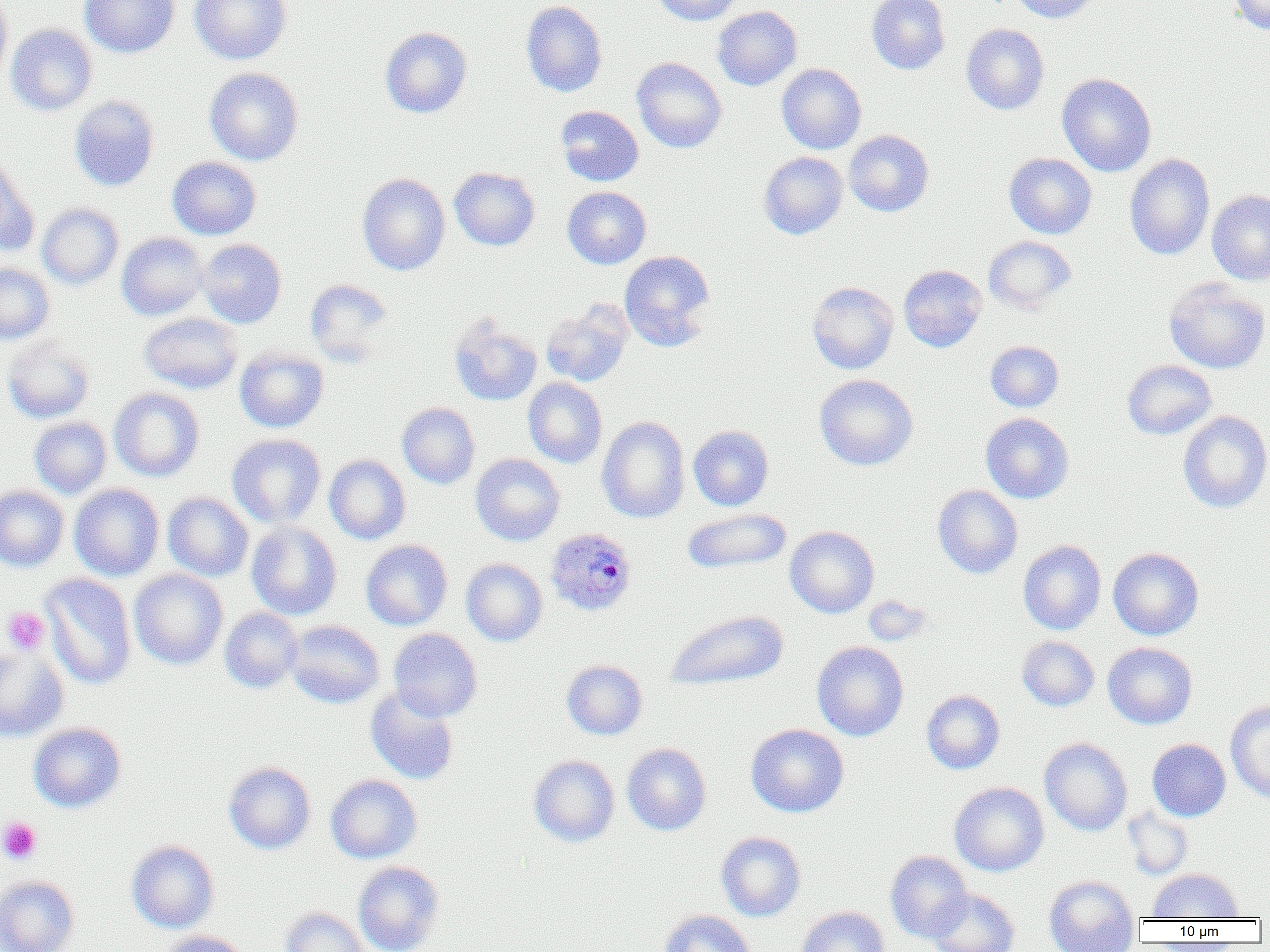

Summary:
  - Coordinate format: approximate bounding boxes as named x1/y1/x2/y2 corners in pixels
  - Uninfected red blood cell locations: (x1=79, y1=0, x2=180, y2=58), (x1=189, y1=0, x2=291, y2=64), (x1=651, y1=0, x2=742, y2=26), (x1=866, y1=0, x2=950, y2=74), (x1=1009, y1=0, x2=1100, y2=23), (x1=1228, y1=0, x2=1270, y2=35), (x1=0, y1=1, x2=13, y2=83), (x1=521, y1=1, x2=607, y2=97), (x1=712, y1=6, x2=802, y2=90), (x1=961, y1=23, x2=1049, y2=115), (x1=5, y1=24, x2=98, y2=116), (x1=379, y1=26, x2=472, y2=118), (x1=631, y1=57, x2=727, y2=153), (x1=777, y1=64, x2=866, y2=154), (x1=203, y1=67, x2=304, y2=166), (x1=1057, y1=73, x2=1157, y2=177), (x1=69, y1=95, x2=159, y2=191), (x1=555, y1=106, x2=643, y2=186), (x1=843, y1=130, x2=934, y2=217), (x1=759, y1=151, x2=848, y2=239), (x1=1004, y1=152, x2=1097, y2=239), (x1=1124, y1=153, x2=1215, y2=260), (x1=0, y1=156, x2=37, y2=256), (x1=167, y1=157, x2=261, y2=240), (x1=448, y1=167, x2=540, y2=250), (x1=357, y1=173, x2=450, y2=275), (x1=562, y1=186, x2=651, y2=269), (x1=1206, y1=190, x2=1270, y2=285), (x1=37, y1=203, x2=123, y2=289), (x1=116, y1=232, x2=209, y2=321), (x1=983, y1=236, x2=1077, y2=314), (x1=197, y1=239, x2=286, y2=328), (x1=619, y1=250, x2=715, y2=351), (x1=0, y1=263, x2=55, y2=345), (x1=899, y1=264, x2=987, y2=352), (x1=1164, y1=278, x2=1270, y2=374), (x1=304, y1=279, x2=395, y2=366), (x1=807, y1=281, x2=899, y2=374), (x1=540, y1=301, x2=632, y2=387), (x1=139, y1=312, x2=244, y2=394), (x1=449, y1=316, x2=542, y2=406), (x1=1, y1=336, x2=95, y2=425), (x1=985, y1=340, x2=1064, y2=412), (x1=234, y1=348, x2=329, y2=432), (x1=1122, y1=360, x2=1217, y2=440), (x1=814, y1=374, x2=918, y2=470), (x1=523, y1=378, x2=607, y2=468), (x1=109, y1=387, x2=205, y2=481), (x1=397, y1=402, x2=480, y2=488), (x1=1178, y1=410, x2=1270, y2=513), (x1=980, y1=413, x2=1074, y2=503), (x1=596, y1=416, x2=690, y2=523), (x1=29, y1=417, x2=112, y2=499), (x1=688, y1=425, x2=774, y2=511), (x1=227, y1=434, x2=326, y2=528), (x1=470, y1=453, x2=565, y2=546), (x1=324, y1=454, x2=410, y2=545), (x1=69, y1=484, x2=164, y2=581), (x1=0, y1=485, x2=69, y2=571), (x1=932, y1=485, x2=1023, y2=578), (x1=163, y1=492, x2=253, y2=581), (x1=681, y1=508, x2=792, y2=574), (x1=246, y1=521, x2=342, y2=620), (x1=785, y1=526, x2=879, y2=618), (x1=361, y1=540, x2=452, y2=630), (x1=1018, y1=540, x2=1106, y2=635), (x1=1108, y1=547, x2=1203, y2=640), (x1=461, y1=558, x2=548, y2=647), (x1=129, y1=569, x2=228, y2=670), (x1=40, y1=573, x2=136, y2=690), (x1=862, y1=595, x2=933, y2=646), (x1=220, y1=608, x2=303, y2=693), (x1=664, y1=609, x2=789, y2=690), (x1=285, y1=620, x2=384, y2=709), (x1=388, y1=628, x2=483, y2=721), (x1=1017, y1=636, x2=1099, y2=711), (x1=812, y1=641, x2=909, y2=741), (x1=1102, y1=642, x2=1198, y2=729), (x1=0, y1=646, x2=69, y2=742), (x1=561, y1=660, x2=648, y2=740), (x1=365, y1=687, x2=460, y2=785), (x1=921, y1=690, x2=1005, y2=774), (x1=1225, y1=700, x2=1270, y2=803), (x1=28, y1=722, x2=126, y2=813), (x1=745, y1=724, x2=849, y2=817), (x1=1039, y1=737, x2=1132, y2=836), (x1=1147, y1=738, x2=1231, y2=821), (x1=622, y1=743, x2=711, y2=835), (x1=528, y1=754, x2=620, y2=847), (x1=223, y1=762, x2=316, y2=854), (x1=326, y1=774, x2=422, y2=863), (x1=949, y1=782, x2=1049, y2=876), (x1=1122, y1=806, x2=1193, y2=879), (x1=716, y1=831, x2=806, y2=921), (x1=126, y1=840, x2=219, y2=933), (x1=885, y1=851, x2=972, y2=943), (x1=352, y1=861, x2=444, y2=952), (x1=1148, y1=869, x2=1242, y2=920), (x1=0, y1=875, x2=79, y2=952), (x1=1044, y1=875, x2=1139, y2=951), (x1=927, y1=888, x2=1020, y2=952), (x1=280, y1=906, x2=370, y2=952), (x1=797, y1=906, x2=889, y2=952), (x1=658, y1=909, x2=756, y2=952), (x1=159, y1=930, x2=251, y2=952)
  - Platelet locations: (x1=2, y1=608, x2=50, y2=654), (x1=0, y1=817, x2=42, y2=864)
  - Plasmodium ovale-infected red blood cell locations: (x1=544, y1=527, x2=637, y2=616)
  - Slide-level diagnosis: Plasmodium ovale
  - Image size: 1270×952 pixels
  - Magnification: 1000x
  - Preparation: thin blood smear
  - Field of view: single
  - Modality: optical microscopy